Report the malaria status of this cell.
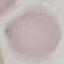

Uninfected.

Photographed with a smartphone camera at the microscope eyepiece. Giemsa stain. Thin smear of blood. Cell patch, automatically extracted from a larger field of view and resized to 64 × 64 pixels.